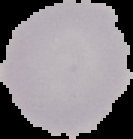 From a thin blood film. Malaria status: uninfected. The area outside the segmented cell region is set to black. Image is 133×139 pixels.